Outline each blood parasite and name the species.
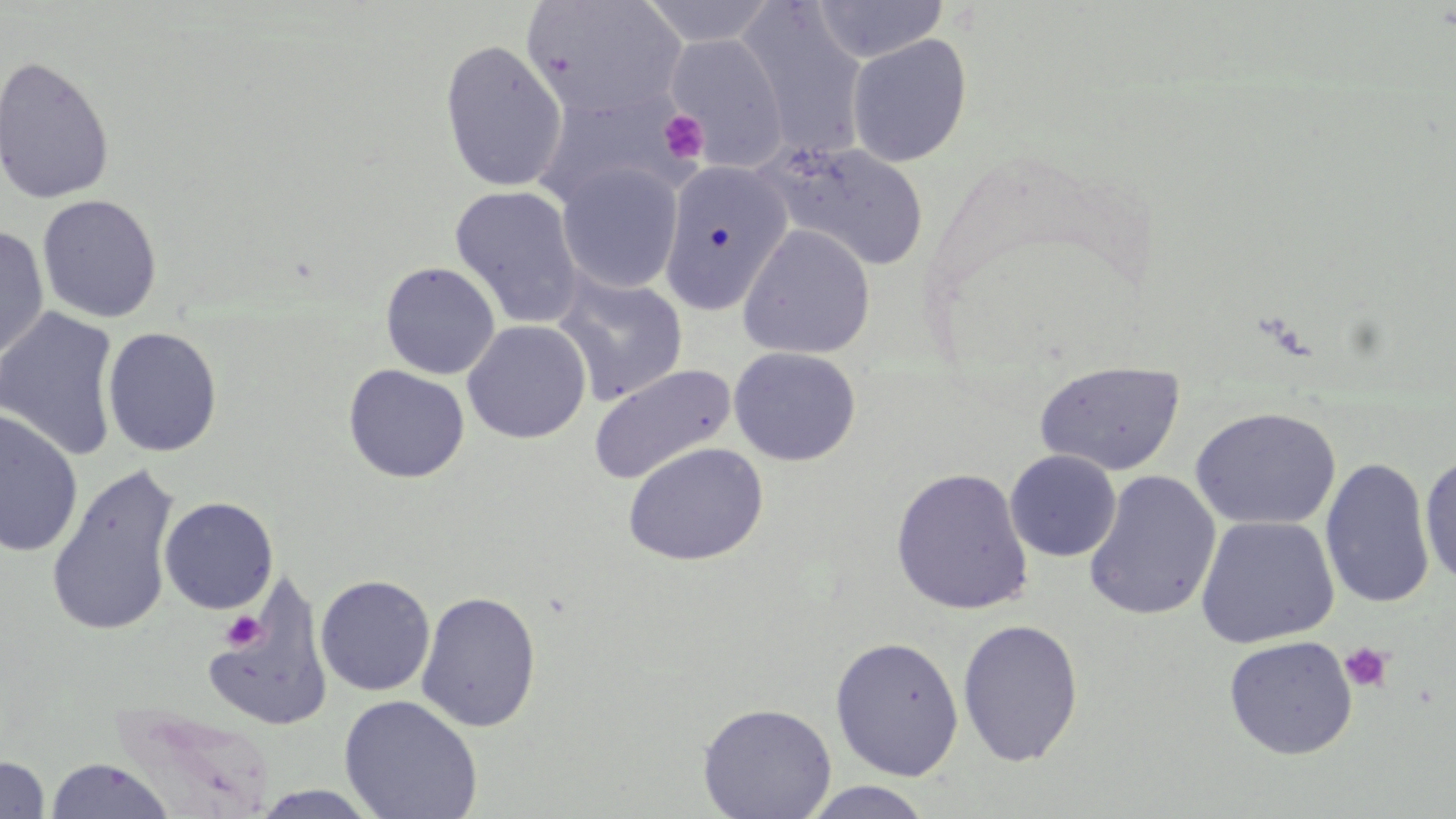
No blood parasites seen.

Approximate bounding boxes as (x1, y1, x2, y2) in pixels. Platelet locations: (657, 109, 710, 165), (220, 611, 266, 652), (1338, 641, 1395, 694). Uninfected red blood cell locations: (521, 0, 687, 121), (639, 0, 778, 47), (811, 0, 948, 63), (737, 3, 868, 160), (664, 33, 788, 171), (846, 34, 973, 167), (439, 39, 567, 193), (0, 54, 116, 206), (534, 87, 693, 210), (767, 142, 931, 274), (660, 160, 792, 316), (556, 163, 684, 294), (449, 185, 584, 329), (37, 195, 162, 323), (738, 224, 875, 359), (0, 227, 50, 362), (380, 261, 500, 380), (553, 275, 688, 405), (0, 305, 121, 462), (462, 320, 591, 444), (102, 326, 223, 457), (728, 347, 861, 466), (1033, 360, 1185, 476), (343, 363, 470, 483), (588, 363, 736, 486), (1190, 406, 1342, 531), (0, 408, 84, 558), (623, 441, 768, 567), (1005, 450, 1121, 562), (1419, 453, 1456, 586), (1320, 457, 1436, 610), (45, 464, 182, 638), (891, 467, 1033, 615), (1083, 470, 1221, 622), (159, 497, 279, 614), (1195, 515, 1339, 649), (315, 574, 435, 697), (203, 575, 333, 733), (416, 590, 542, 732), (957, 619, 1084, 767), (829, 635, 964, 780), (1223, 635, 1358, 760), (339, 694, 483, 818), (697, 702, 837, 818), (111, 706, 276, 818), (0, 756, 50, 818), (44, 758, 176, 818), (799, 782, 936, 818), (247, 786, 383, 819). Slide-level diagnosis: negative for blood parasites. Optical microscopy. May-Grünwald-Giemsa-stained preparation. Image is 1456×819 pixels. Thin blood smear. One field of a larger specimen. Captured at 1000x magnification.